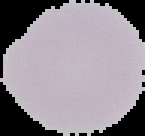

Summary:
  - Image size: 145×136 pixels
  - Preparation: thin blood smear
  - Result: no malaria parasites detected
  - Image type: segmented cell region with the area outside set to black